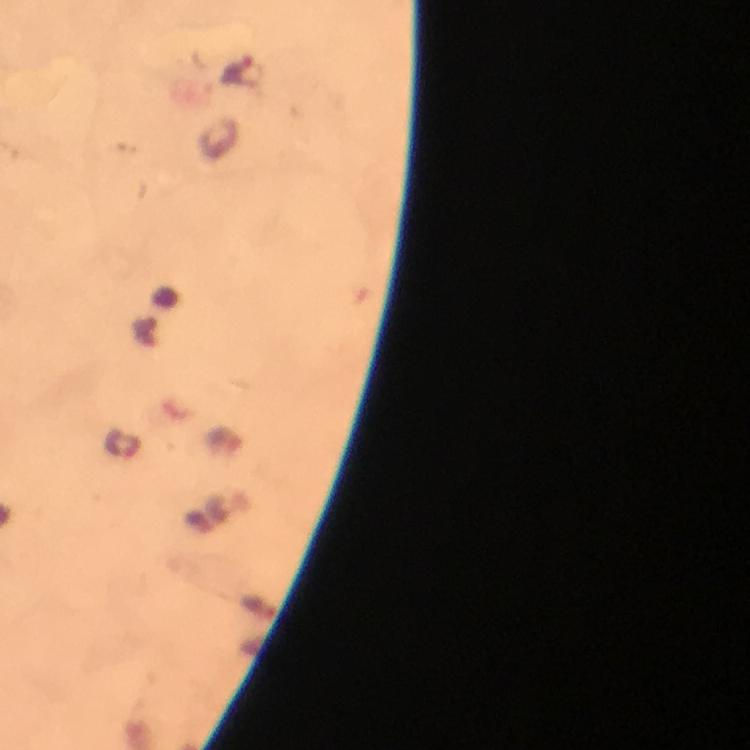

Approximate centers as [x, y] in pixels.
Summary:
  - Malaria parasite locations: [245, 71]
  - Image size: 750×750 pixels
  - Capture: smartphone camera through the microscope
  - Context: from a diagnostic examination for malaria
  - Immersion oil: applied
  - Magnification: 100x
  - Preparation: thick smear
  - Cropped from: a single field of view
  - Stain: Giemsa